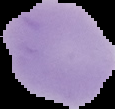
From a thin blood film. Image is 115×109 pixels. Malaria status: uninfected. The area outside the segmented cell region is set to black.